Give the position of every leukocyte visible.
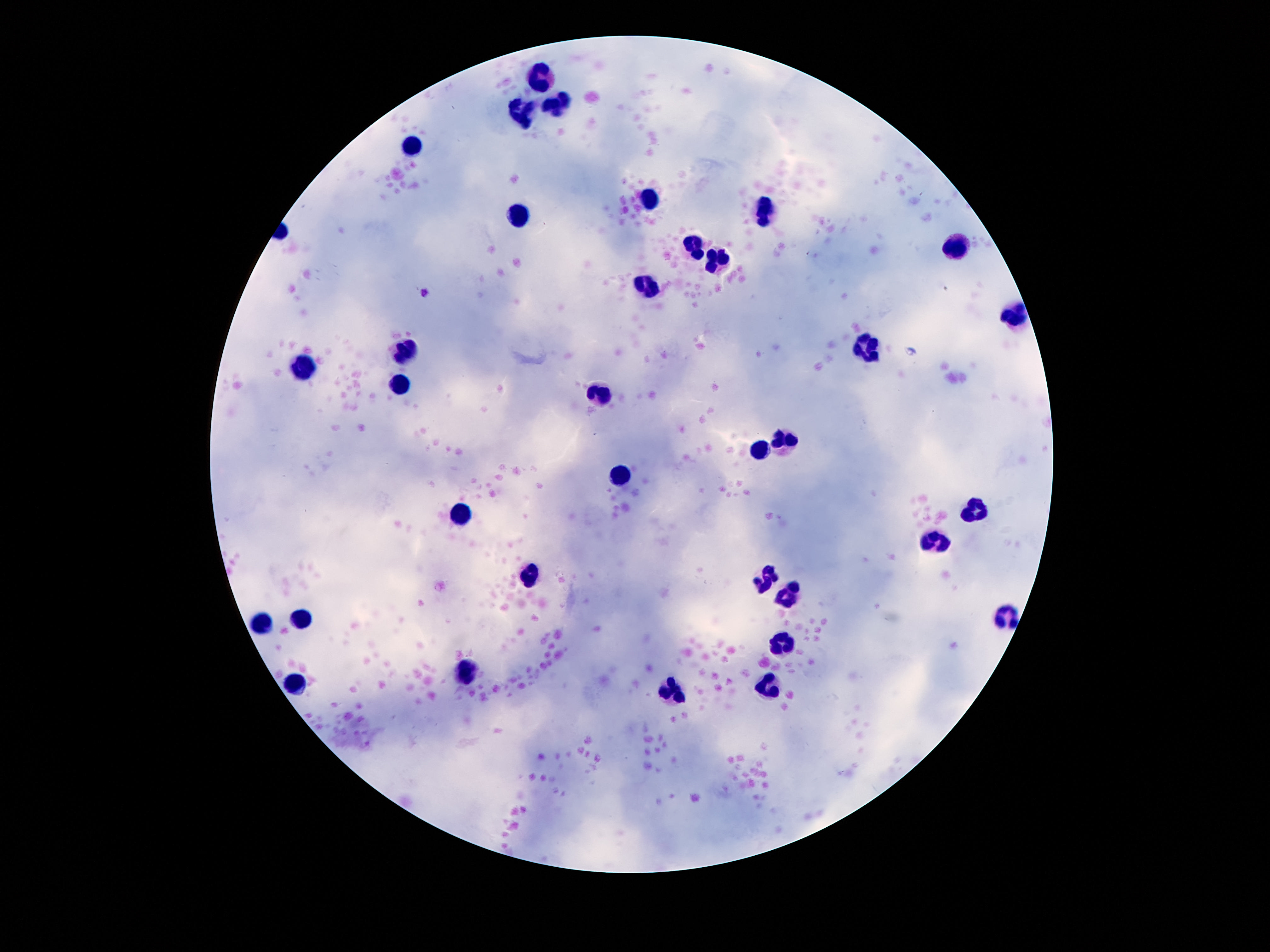

Approximate centers as (x, y) in pixels.
Leukocytes: (544, 78), (555, 100), (524, 111), (410, 147), (651, 198), (766, 209), (520, 216), (954, 245), (692, 248), (715, 260), (644, 290), (1011, 316), (869, 348), (405, 354), (303, 366), (401, 386), (600, 392), (783, 439), (759, 450), (618, 478), (975, 510), (461, 512), (936, 541), (529, 573), (766, 581), (795, 585), (785, 598), (302, 616), (1005, 616), (262, 624), (783, 646), (470, 670), (297, 685), (768, 687), (673, 692).

Summary:
  - Magnification: 100x
  - Field of view: single
  - Capture: smartphone camera through the microscope eyepiece
  - Stain: Giemsa
  - Image size: 1270×952 pixels
  - Preparation: thick blood smear
  - Patient malaria status: not infected